State which parasite is depicted.
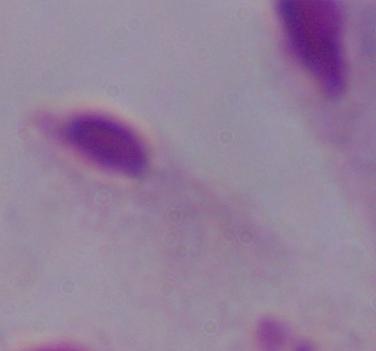
A trichomonad.

1000x magnification. Photomicrograph.